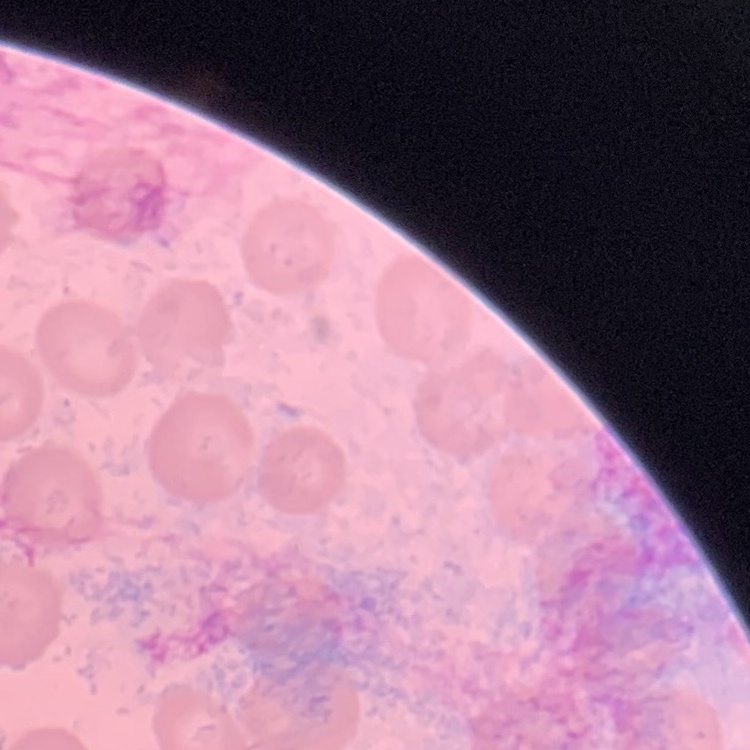

The erythrocytes show no rouleaux formation. One tile cut from a larger photomicrograph. Stained with either Field's or Giemsa. Thin peripheral smear.